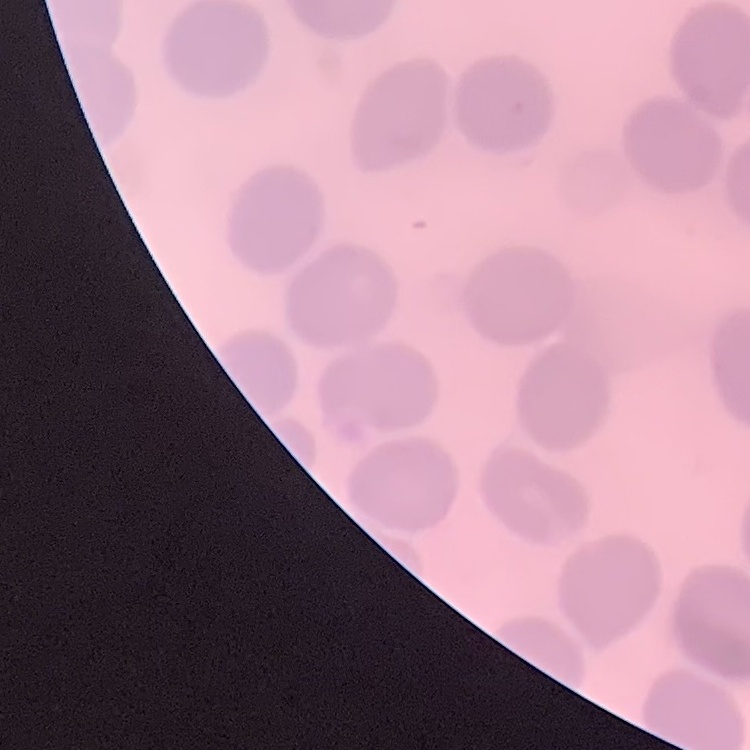

red blood cell morphology = no rouleaux formation
preparation = thin blood smear
image type = one tile cut from a larger photomicrograph
stain = Field's or Giemsa